Report the malaria status.
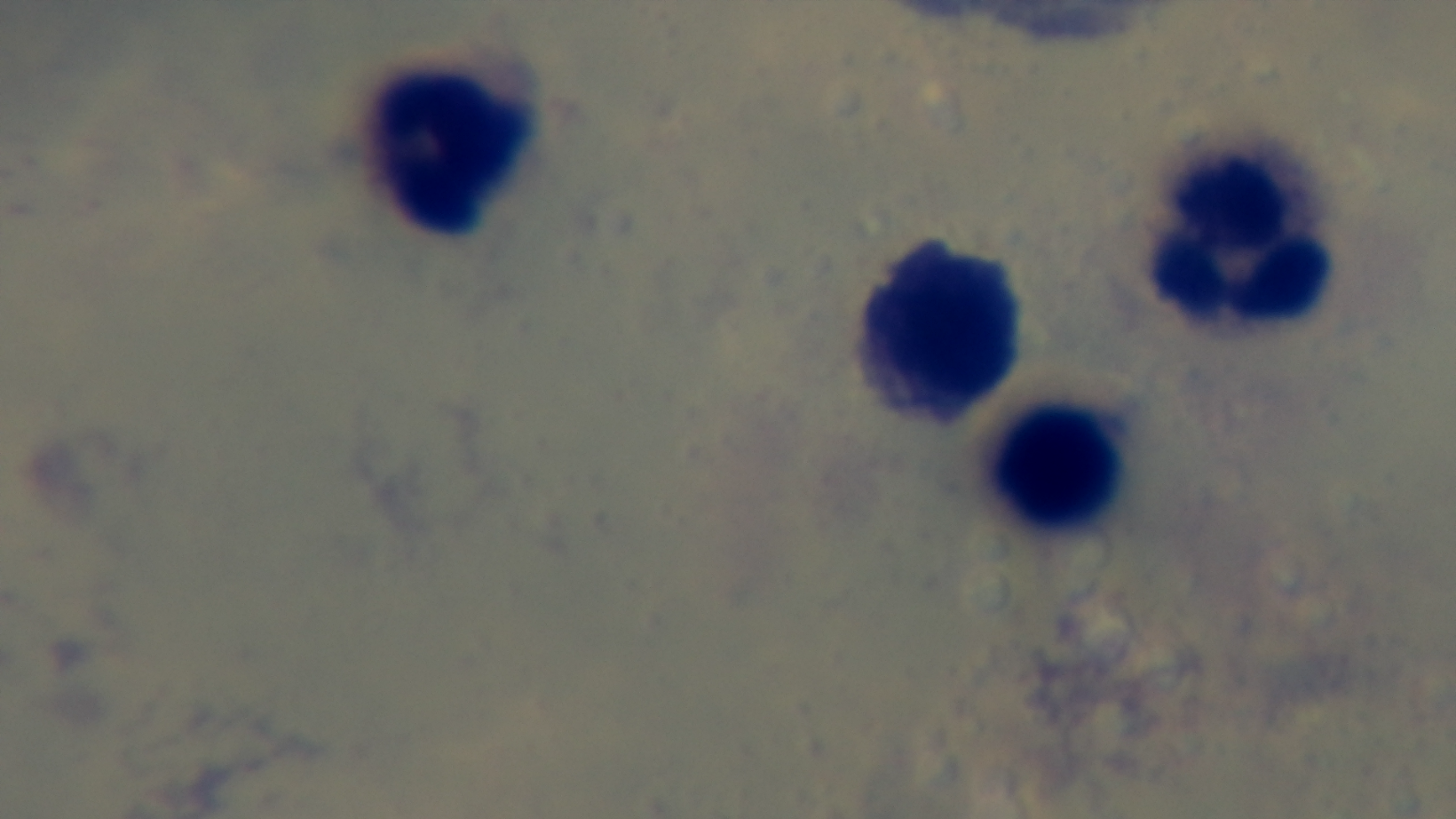

It is uninfected.

Summary:
  - Stain: Giemsa
  - Objective: 100x oil immersion
  - Field of view: one from the slide
  - Capture: mounted 4K digital camera
  - Modality: light microscopy
  - Preparation: thick